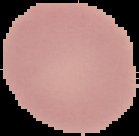

preparation = thin blood film
result = no Plasmodium parasites seen
image type = segmented cell region with the area outside set to black
image size = 139×136 pixels